Assess the morphology of the red blood cells.
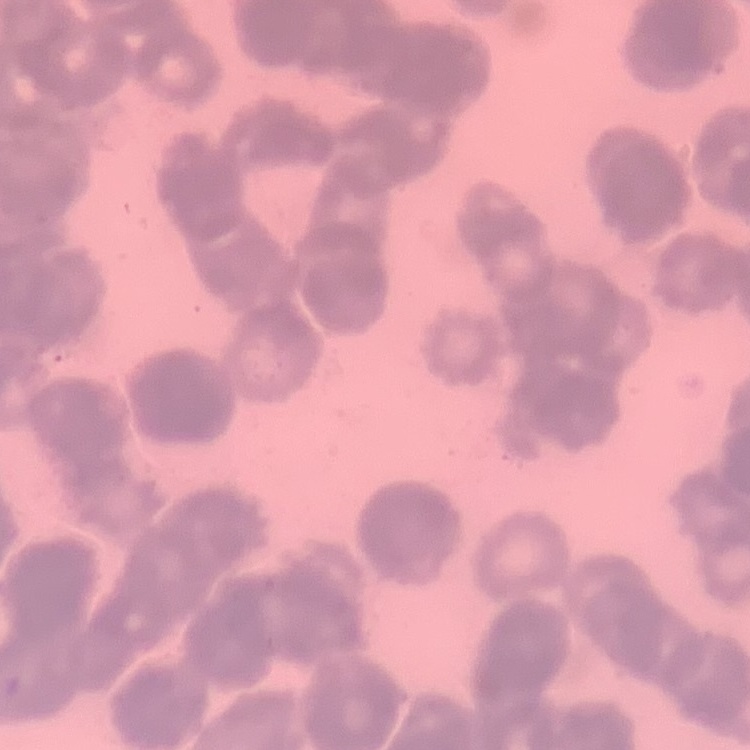
They show rouleaux formation.

{
  "image_type": "one tile cut from a larger photomicrograph",
  "preparation": "thin blood smear",
  "stain": "Field's or Giemsa"
}